Identify the preparation type.
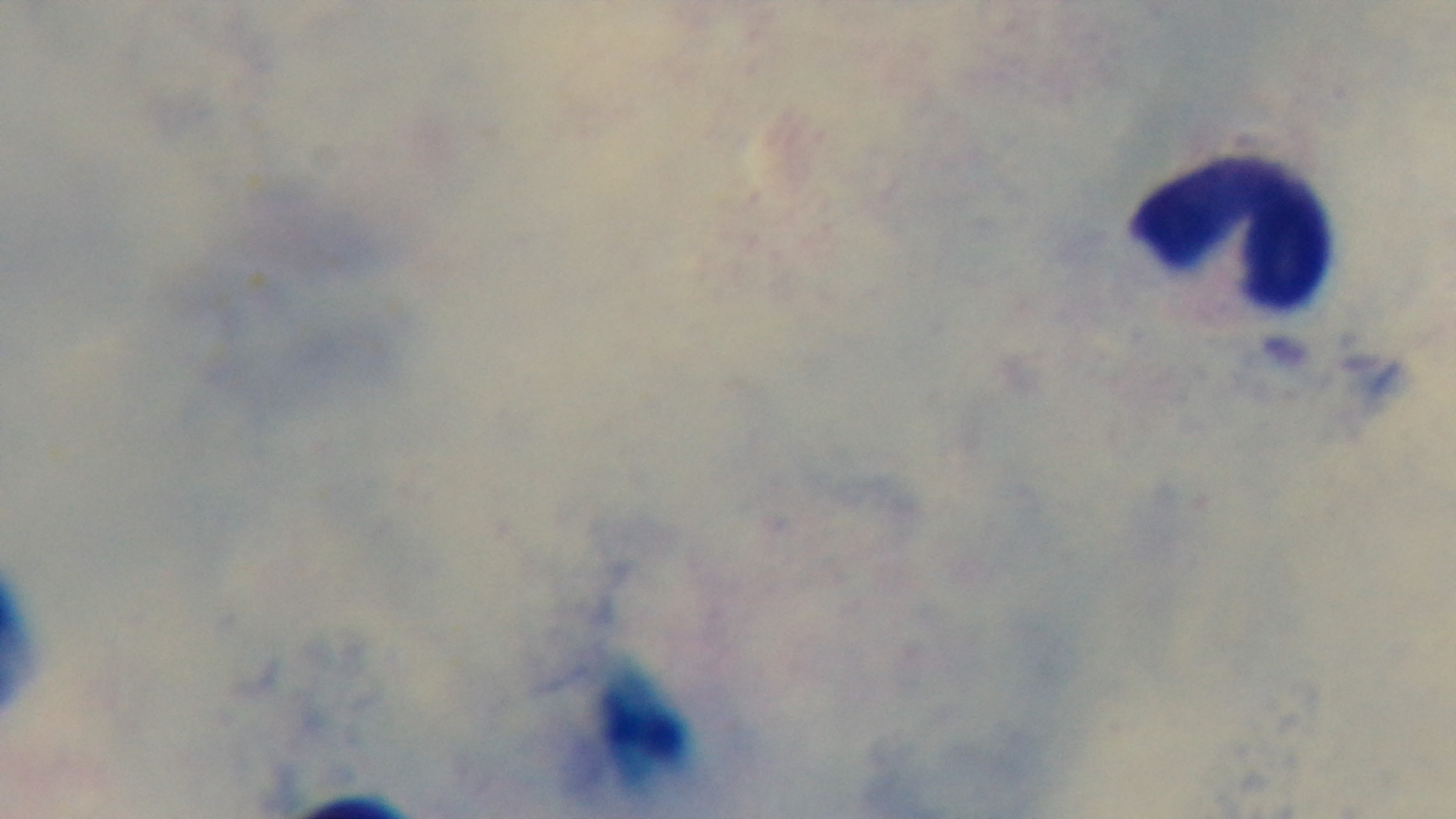
Thick.

Summary:
  - Stain: Giemsa
  - Field of view: single
  - Capture: mounted 4K digital camera
  - Malaria status: uninfected
  - Modality: light microscopy
  - Objective: 100x oil immersion